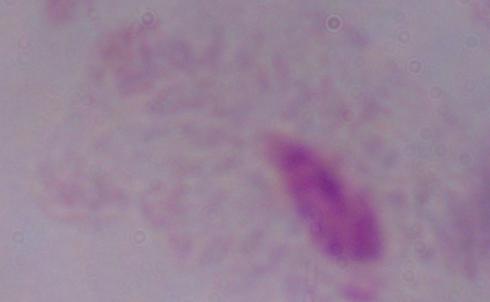

Summary:
  - Magnification: 1000x
  - Modality: micrograph
  - Identification: trichomonad